Name the blood parasite species.
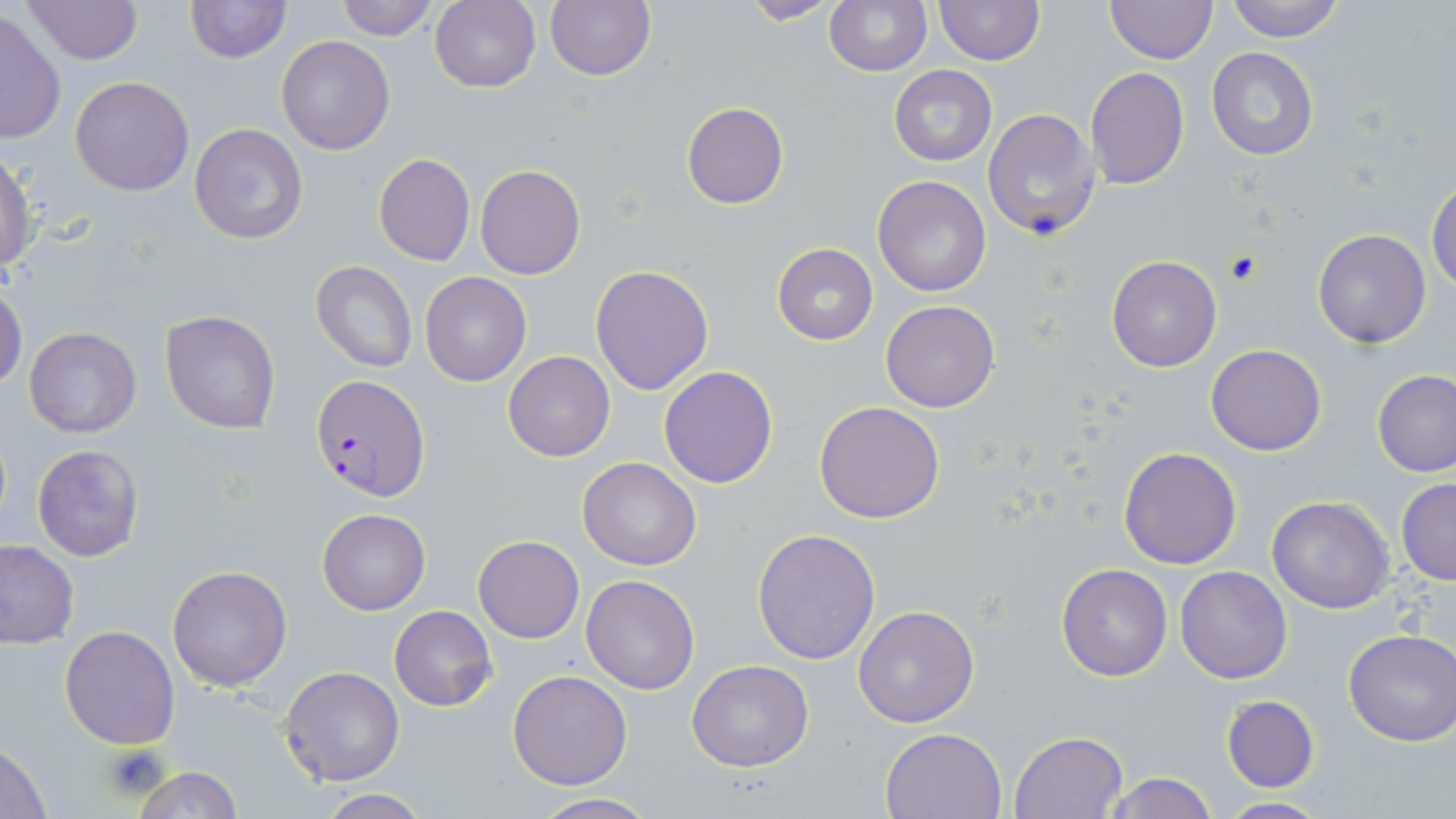
Plasmodium falciparum.

{
  "stain": "May-Grünwald-Giemsa",
  "plasmodium_falciparum_infected_red_blood_cell_locations": "approximate bounding boxes as (x1,y1)-(x2,y2) corner pairs in pixels: (310,373)-(432,504)",
  "uninfected_red_blood_cell_locations": "approximate bounding boxes as (x1,y1)-(x2,y2) corner pairs in pixels: (19,0)-(143,67), (185,0)-(289,64), (333,0)-(439,40), (430,0)-(541,93), (740,0)-(843,25), (825,0)-(931,76), (934,0)-(1044,66), (1105,0)-(1217,64), (1223,0)-(1348,42), (543,1)-(657,82), (1,11)-(67,143), (275,36)-(395,155), (1206,47)-(1319,161), (888,65)-(996,165), (1085,66)-(1188,189), (70,76)-(194,197), (682,102)-(788,209), (983,108)-(1103,240), (190,123)-(308,244), (0,152)-(36,273), (372,152)-(475,267), (475,165)-(586,280), (872,174)-(993,296), (1427,177)-(1456,293), (1312,229)-(1432,348), (772,243)-(878,345), (1105,255)-(1221,373), (311,259)-(417,372), (589,264)-(714,396), (420,272)-(532,386), (0,284)-(25,395), (880,300)-(1000,412), (160,310)-(282,435), (23,325)-(142,439), (1206,343)-(1326,456), (503,351)-(615,461), (659,366)-(779,487), (1373,370)-(1456,477), (814,401)-(944,522), (32,444)-(144,562), (1118,447)-(1242,570), (579,457)-(701,570), (1396,478)-(1456,585), (1267,496)-(1394,613), (316,506)-(431,615), (752,528)-(881,665), (474,536)-(584,643), (0,539)-(79,648), (1056,564)-(1173,681), (167,565)-(292,691), (1175,565)-(1292,683), (581,574)-(700,694), (852,605)-(980,729), (389,606)-(496,711), (59,625)-(179,748), (1343,630)-(1456,747), (687,659)-(813,771), (279,666)-(405,787), (507,669)-(633,789), (1220,694)-(1321,794), (879,727)-(1007,819), (1009,730)-(1127,818), (0,740)-(51,817), (130,766)-(244,818), (1101,773)-(1220,819), (315,791)-(431,818), (526,793)-(659,818), (1214,797)-(1332,817)",
  "platelet_locations": "approximate bounding boxes as (x1,y1)-(x2,y2) corner pairs in pixels: (1222,252)-(1263,285), (103,744)-(168,796)",
  "magnification": "1000x",
  "preparation": "thin blood smear",
  "field_of_view": "one of a larger specimen",
  "image_size": "1456×819 pixels",
  "modality": "light microscopy"
}